Assess this cell for malaria.
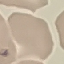

It is uninfected.

Thin smear of blood. Acquired by smartphone through the microscope eyepiece. Automatically extracted cell patch, resized to 64 × 64 pixels. Giemsa stain.